Name the parasite shown.
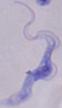
This is a trypanosome.

Captured at 1000x magnification. Photomicrograph.